Locate every leukocyte (white blood cell).
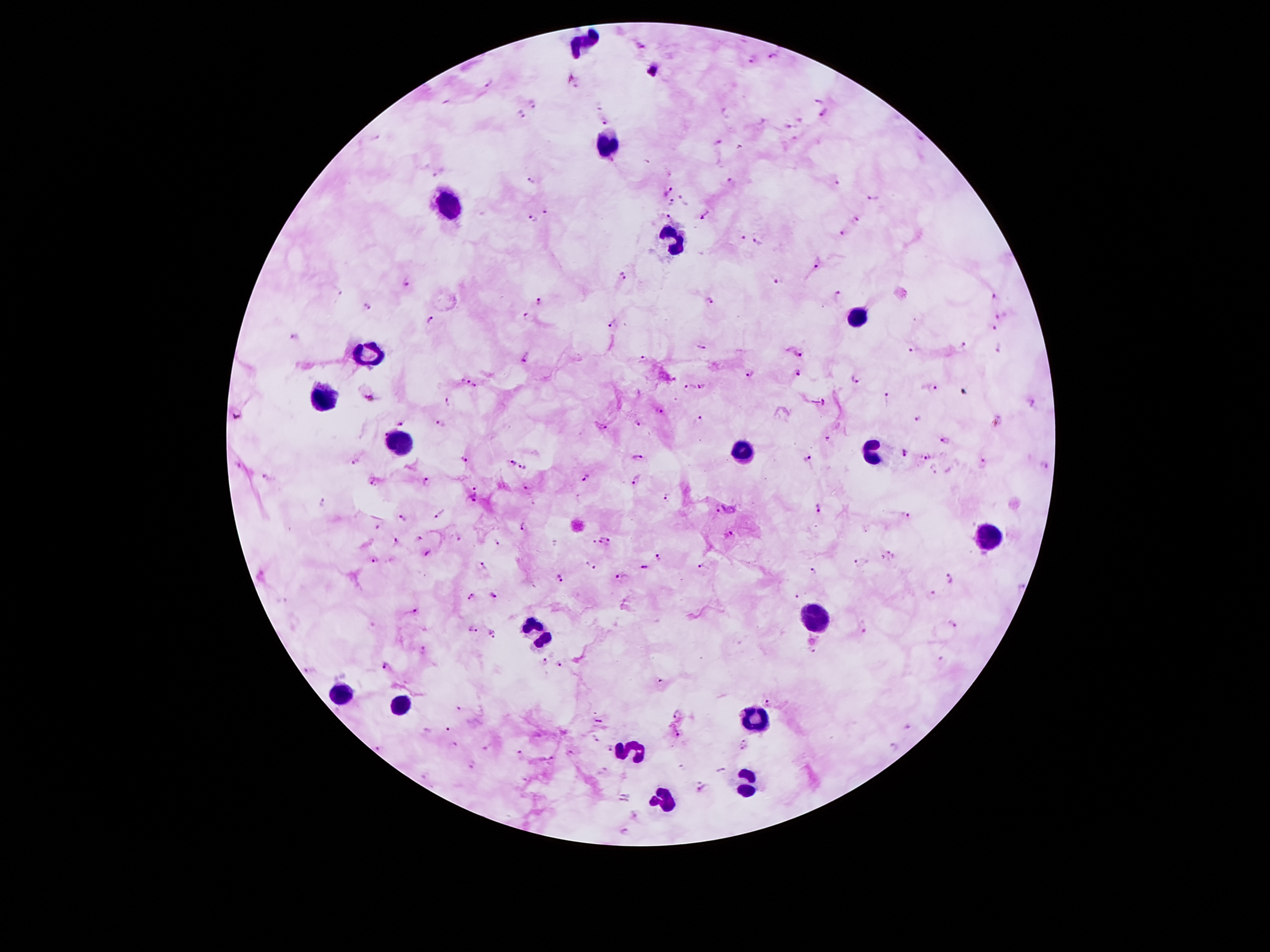

Approximate centers as (x, y) in pixels.
Leukocytes: (581, 43), (605, 145), (450, 195), (673, 238), (857, 318), (363, 350), (324, 395), (400, 445), (876, 447), (743, 451), (986, 535), (812, 617), (538, 627), (337, 692), (400, 703), (755, 717), (630, 752), (747, 782), (663, 799).

Malaria parasite locations: (773, 57), (752, 60), (651, 72), (490, 85), (818, 100), (533, 105), (825, 113), (522, 115), (606, 118), (788, 127), (377, 137), (718, 143), (439, 174), (532, 179), (838, 182), (732, 184), (669, 190), (874, 197), (685, 199), (670, 202), (546, 212), (670, 217), (706, 217), (533, 219), (857, 220), (843, 233), (743, 238), (759, 244), (817, 262), (623, 275), (776, 281), (406, 283), (837, 295), (995, 296), (711, 300), (539, 301), (366, 308), (998, 317), (527, 318), (430, 320), (613, 323), (994, 329), (293, 336), (702, 347), (962, 347), (998, 347), (913, 351), (798, 354), (526, 358), (642, 359), (799, 372), (750, 375), (464, 379), (855, 379), (703, 386), (478, 388), (933, 389), (688, 390), (888, 397), (370, 398), (824, 401), (448, 402), (1034, 403), (659, 409), (698, 419), (917, 420), (403, 423), (441, 423), (637, 425), (603, 428), (384, 431), (828, 438), (945, 441), (904, 453), (926, 456), (637, 457), (808, 458), (464, 459), (357, 463), (511, 463), (983, 465), (1045, 465), (521, 468), (935, 469), (267, 476), (586, 477), (635, 481), (428, 482), (373, 483), (528, 486), (475, 488), (668, 499), (473, 501), (323, 504), (819, 508), (718, 509), (441, 514), (906, 515), (403, 519), (524, 527), (732, 534), (419, 537), (458, 538), (601, 540), (396, 541), (611, 541), (498, 544), (593, 545), (891, 553), (428, 554), (657, 558), (374, 561), (590, 564), (857, 564), (483, 565), (702, 565), (644, 568), (814, 570), (621, 577), (559, 578), (952, 579), (1020, 587), (494, 595), (471, 597), (797, 597), (416, 611), (952, 624), (473, 628), (863, 630), (491, 634), (812, 651), (423, 652), (545, 661), (559, 663), (387, 666), (310, 672), (660, 681), (768, 701), (460, 710), (677, 715), (600, 720), (448, 729), (678, 737), (596, 738), (745, 740), (455, 745), (485, 747), (609, 748), (743, 748), (892, 748), (378, 749), (571, 754), (519, 755), (553, 758), (473, 765), (703, 788), (636, 817), (626, 831). Photographed through the microscope eyepiece with a smartphone camera. Image is 1270×952 pixels. One field from this slide. Thick peripheral-blood smear. Patient malaria status: infected with Plasmodium falciparum. Giemsa-stained preparation. 100x magnification.